Report the malaria status of this cell.
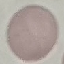

Uninfected.

Summary:
  - Image type: cell patch, automatically extracted from a larger field of view and resized to 64 × 64 pixels
  - Preparation: thin blood film
  - Capture: smartphone camera at the microscope eyepiece
  - Stain: Giemsa